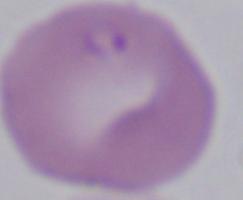

magnification = 1000x
modality = micrograph
identification = Babesia